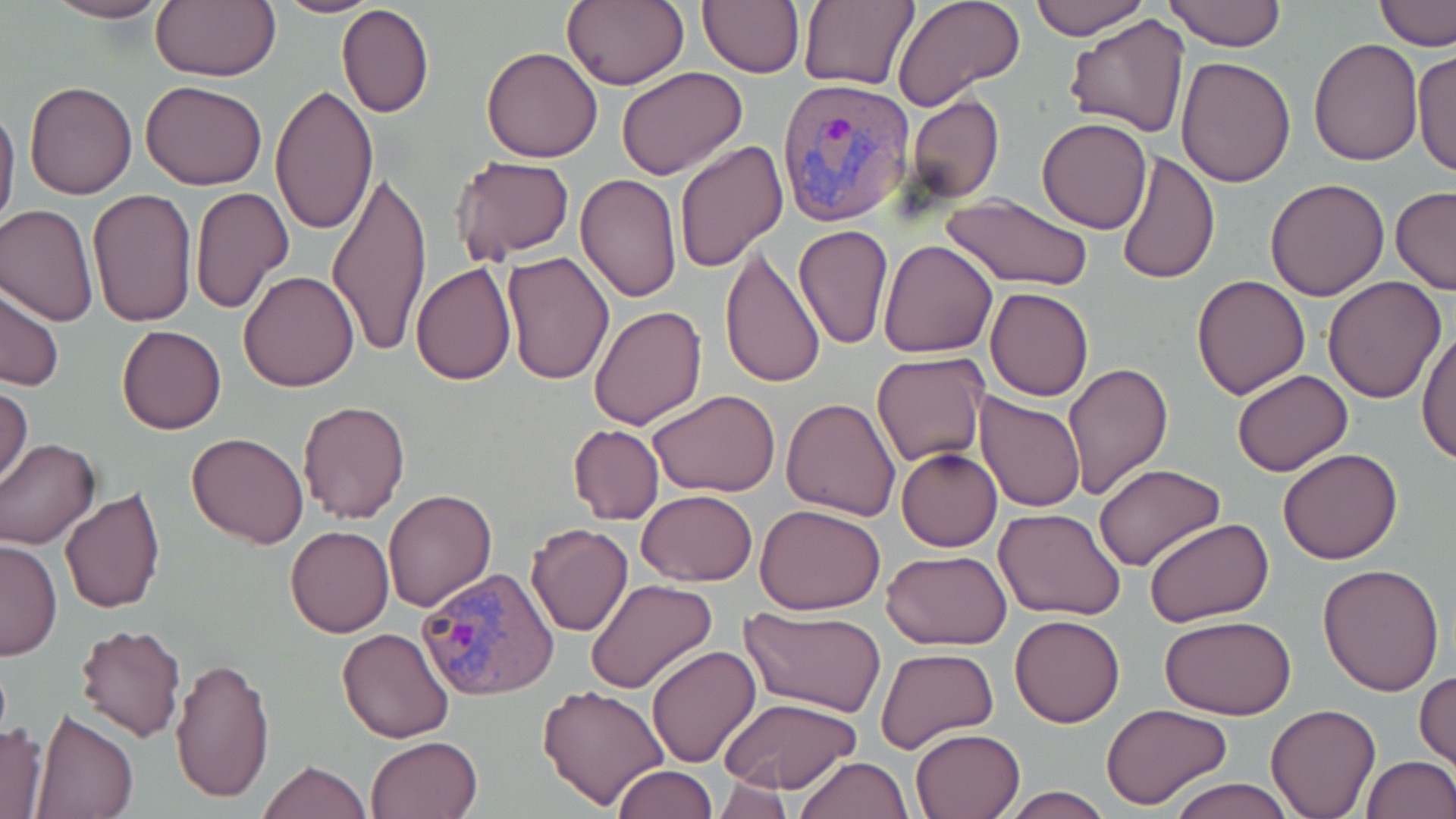
slide-level diagnosis = Plasmodium vivax
magnification = 1000x
stain = May-Grünwald-Giemsa
field of view = one of a larger specimen
image size = 1456×819 pixels
preparation = thin blood film
uninfected red blood cell locations = approximate bounding boxes as (x1, y1, x2, y2) in pixels: (45, 0, 170, 23), (150, 0, 279, 83), (271, 0, 387, 17), (564, 0, 690, 90), (698, 0, 804, 77), (798, 0, 918, 90), (1029, 0, 1148, 39), (1164, 0, 1286, 51), (1374, 0, 1456, 51), (894, 1, 1023, 113), (337, 2, 435, 118), (1065, 11, 1190, 136), (1308, 37, 1424, 166), (481, 46, 604, 162), (1410, 46, 1455, 180), (1174, 55, 1297, 188), (616, 66, 748, 181), (140, 80, 267, 191), (24, 81, 137, 199), (268, 83, 377, 237), (905, 95, 1004, 205), (0, 98, 20, 240), (1037, 116, 1152, 233), (673, 139, 789, 272), (1117, 149, 1221, 287), (450, 155, 575, 264), (327, 169, 430, 360), (575, 175, 681, 302), (1265, 177, 1391, 300), (1390, 185, 1456, 296), (85, 187, 197, 327), (189, 187, 293, 313), (938, 192, 1094, 293), (0, 205, 98, 327), (792, 226, 893, 348), (878, 238, 998, 358), (719, 246, 826, 392), (500, 251, 614, 384), (410, 262, 518, 385), (237, 270, 361, 392), (1191, 274, 1310, 399), (1322, 276, 1448, 403), (0, 286, 65, 393), (985, 286, 1094, 402), (589, 304, 707, 429), (116, 324, 227, 434), (1417, 326, 1456, 467), (871, 353, 989, 466), (1063, 363, 1174, 500), (1232, 369, 1354, 476), (0, 384, 33, 493), (648, 387, 780, 496), (977, 393, 1086, 513), (782, 397, 901, 522), (298, 399, 411, 523), (567, 424, 664, 527), (186, 431, 310, 548), (0, 437, 101, 549), (1278, 447, 1404, 565), (896, 448, 1002, 551), (1094, 462, 1223, 570), (60, 486, 167, 613), (384, 487, 497, 611), (636, 491, 758, 587), (755, 503, 885, 615), (995, 508, 1129, 621), (1144, 517, 1275, 625), (524, 522, 632, 638), (286, 526, 394, 638), (0, 538, 61, 661), (882, 549, 1014, 650), (1317, 563, 1445, 697), (586, 578, 716, 694), (742, 607, 886, 717), (1009, 613, 1125, 727), (1158, 617, 1298, 720), (74, 624, 186, 743), (335, 628, 455, 744), (645, 645, 761, 768), (876, 647, 998, 753), (170, 654, 276, 804), (1414, 670, 1456, 771), (539, 682, 671, 811), (719, 696, 862, 796), (1100, 703, 1232, 810), (1265, 703, 1381, 818), (31, 711, 139, 819), (0, 722, 49, 818), (911, 728, 1024, 818), (366, 735, 481, 819), (793, 756, 912, 819), (1361, 756, 1455, 819), (258, 761, 370, 819), (613, 764, 719, 819), (1164, 778, 1300, 819), (710, 782, 800, 819), (996, 786, 1113, 819)
Plasmodium vivax-infected red blood cell locations = approximate bounding boxes as (x1, y1, x2, y2) in pixels: (779, 77, 917, 226), (416, 568, 560, 702)
modality = optical microscopy